Locate every blood parasite and identify its species.
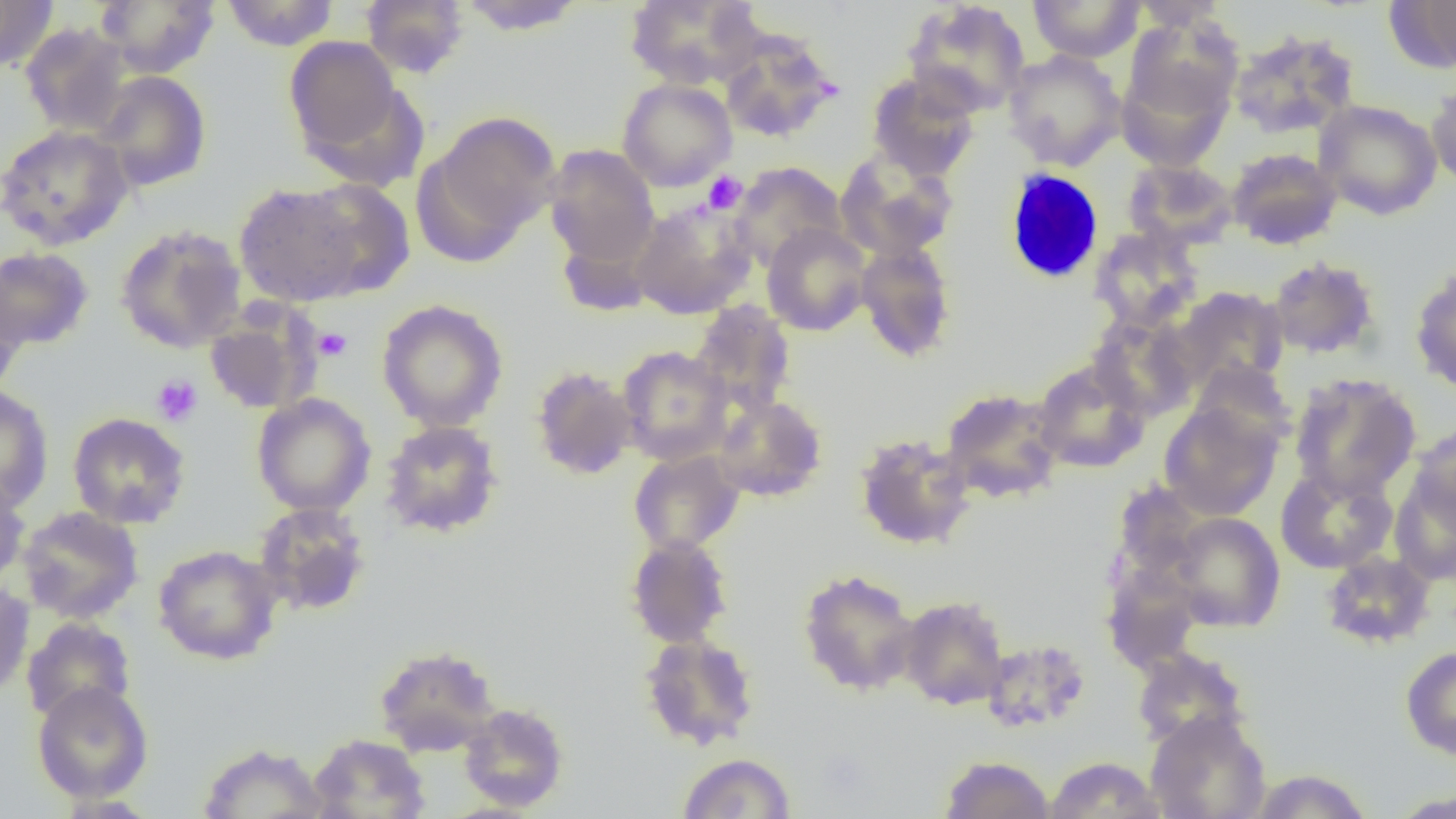
No blood parasites seen.

Approximate bounding boxes as named x1/y1/x2/y2 corners in pixels. Uninfected red blood cell locations: (x1=96, y1=0, x2=220, y2=78), (x1=221, y1=0, x2=339, y2=51), (x1=361, y1=0, x2=469, y2=79), (x1=456, y1=0, x2=587, y2=36), (x1=623, y1=0, x2=764, y2=90), (x1=901, y1=0, x2=1031, y2=117), (x1=1028, y1=0, x2=1144, y2=62), (x1=1129, y1=0, x2=1232, y2=30), (x1=1386, y1=0, x2=1456, y2=74), (x1=0, y1=1, x2=59, y2=72), (x1=1123, y1=16, x2=1243, y2=128), (x1=19, y1=22, x2=132, y2=137), (x1=1228, y1=29, x2=1360, y2=139), (x1=719, y1=30, x2=840, y2=143), (x1=283, y1=35, x2=405, y2=162), (x1=1003, y1=49, x2=1126, y2=170), (x1=1117, y1=53, x2=1237, y2=172), (x1=93, y1=71, x2=211, y2=192), (x1=866, y1=72, x2=981, y2=181), (x1=617, y1=78, x2=736, y2=191), (x1=1426, y1=79, x2=1456, y2=191), (x1=1314, y1=99, x2=1442, y2=220), (x1=421, y1=111, x2=561, y2=256), (x1=0, y1=124, x2=134, y2=250), (x1=544, y1=145, x2=659, y2=267), (x1=1227, y1=147, x2=1342, y2=249), (x1=834, y1=150, x2=960, y2=262), (x1=1123, y1=159, x2=1238, y2=250), (x1=729, y1=162, x2=847, y2=270), (x1=298, y1=178, x2=416, y2=299), (x1=233, y1=182, x2=366, y2=306), (x1=630, y1=198, x2=758, y2=319), (x1=761, y1=223, x2=871, y2=336), (x1=115, y1=224, x2=247, y2=353), (x1=1089, y1=225, x2=1203, y2=333), (x1=855, y1=241, x2=957, y2=362), (x1=0, y1=246, x2=94, y2=350), (x1=1267, y1=256, x2=1381, y2=359), (x1=1410, y1=267, x2=1456, y2=394), (x1=0, y1=280, x2=27, y2=399), (x1=1171, y1=286, x2=1288, y2=392), (x1=376, y1=299, x2=509, y2=432), (x1=689, y1=301, x2=797, y2=416), (x1=204, y1=305, x2=320, y2=415), (x1=1089, y1=313, x2=1200, y2=422), (x1=616, y1=345, x2=734, y2=465), (x1=1032, y1=359, x2=1150, y2=473), (x1=1187, y1=359, x2=1297, y2=453), (x1=530, y1=365, x2=639, y2=480), (x1=1289, y1=373, x2=1421, y2=500), (x1=0, y1=385, x2=54, y2=510), (x1=940, y1=388, x2=1065, y2=504), (x1=251, y1=393, x2=376, y2=517), (x1=713, y1=394, x2=828, y2=502), (x1=1159, y1=401, x2=1282, y2=520), (x1=67, y1=412, x2=191, y2=529), (x1=379, y1=420, x2=503, y2=538), (x1=1410, y1=422, x2=1456, y2=525), (x1=854, y1=432, x2=976, y2=551), (x1=628, y1=449, x2=745, y2=556), (x1=1274, y1=465, x2=1398, y2=574), (x1=0, y1=472, x2=31, y2=588), (x1=1389, y1=472, x2=1456, y2=586), (x1=1112, y1=482, x2=1208, y2=587), (x1=253, y1=502, x2=372, y2=616), (x1=17, y1=506, x2=144, y2=624), (x1=1167, y1=512, x2=1286, y2=632), (x1=625, y1=534, x2=734, y2=648), (x1=153, y1=544, x2=283, y2=665), (x1=1320, y1=551, x2=1437, y2=649), (x1=1101, y1=563, x2=1204, y2=673), (x1=797, y1=568, x2=921, y2=697), (x1=0, y1=579, x2=34, y2=697), (x1=898, y1=595, x2=1010, y2=710), (x1=21, y1=617, x2=137, y2=726), (x1=638, y1=631, x2=760, y2=751), (x1=981, y1=638, x2=1092, y2=734), (x1=373, y1=644, x2=501, y2=757), (x1=1400, y1=645, x2=1456, y2=760), (x1=1131, y1=647, x2=1250, y2=750), (x1=32, y1=680, x2=154, y2=803), (x1=459, y1=703, x2=569, y2=812), (x1=1145, y1=710, x2=1271, y2=819), (x1=308, y1=733, x2=431, y2=819), (x1=198, y1=742, x2=330, y2=819), (x1=677, y1=752, x2=796, y2=818), (x1=939, y1=755, x2=1054, y2=819), (x1=1044, y1=756, x2=1165, y2=819), (x1=1248, y1=768, x2=1374, y2=818), (x1=1387, y1=789, x2=1456, y2=818). White blood cell locations: (x1=1003, y1=168, x2=1106, y2=285). Platelet locations: (x1=703, y1=171, x2=747, y2=214), (x1=313, y1=327, x2=352, y2=361), (x1=151, y1=374, x2=203, y2=426). Slide-level diagnosis: no evidence of blood parasites. Light microscopy. Image is 1456×819 pixels. Thin blood smear. 1000x magnification. One field of a larger specimen.